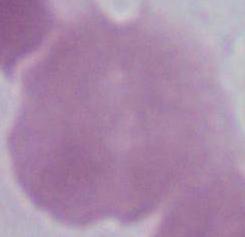

magnification = 1000x
modality = micrograph
identification = erythrocyte